Assess this cell for malaria.
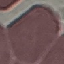
Uninfected.

image type = cell patch, automatically extracted from a larger field of view and resized to 64 × 64 pixels
preparation = thin blood smear
stain = Giemsa
capture = smartphone camera at the microscope eyepiece